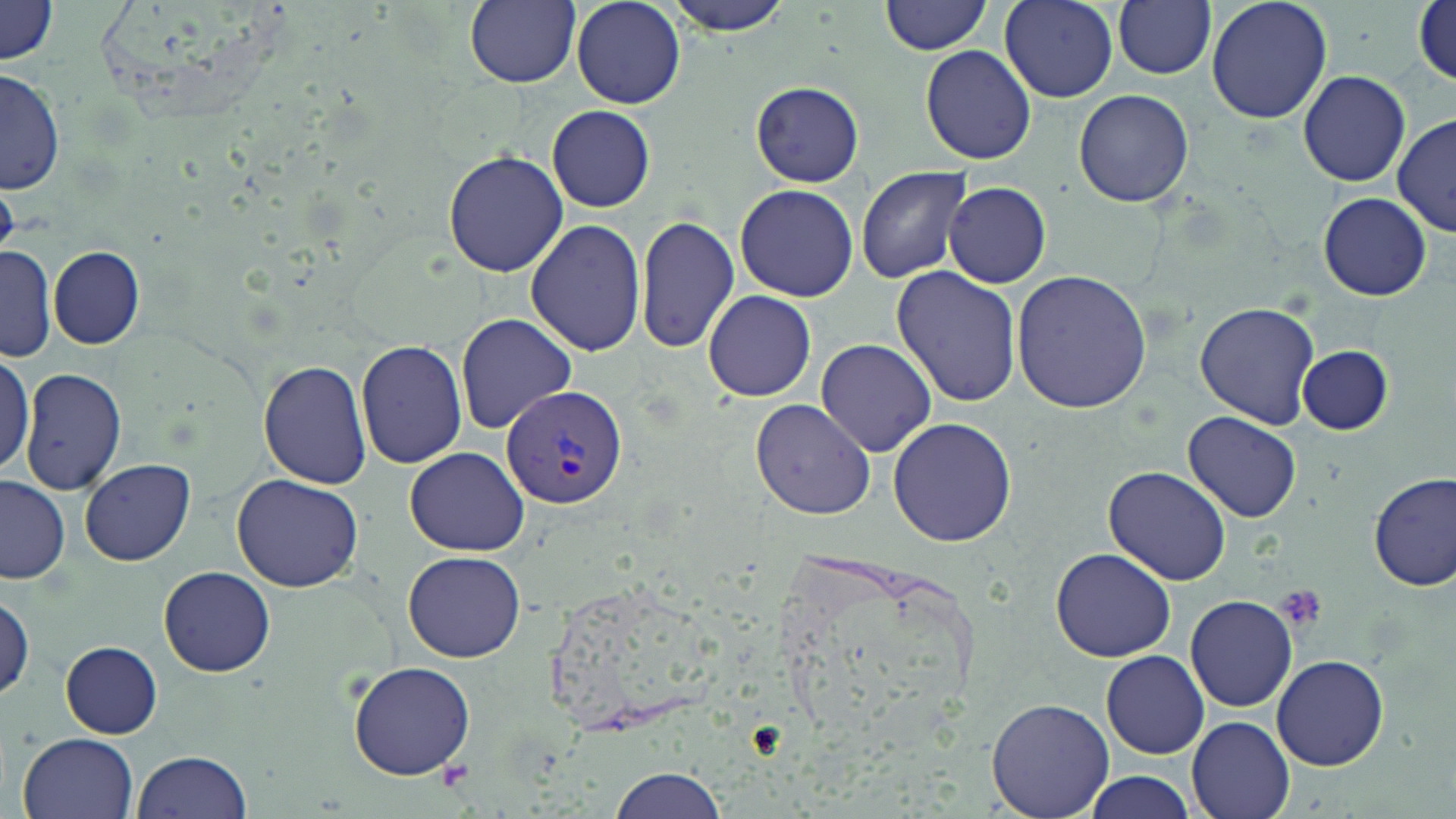

Approximate bounding boxes as named x1/y1/x2/y2 corners in pixels. Platelet locations: (x1=1271, y1=584, x2=1326, y2=632), (x1=436, y1=760, x2=474, y2=791). Plasmodium vivax-infected red blood cell locations: (x1=503, y1=384, x2=627, y2=507). Uninfected red blood cell locations: (x1=464, y1=0, x2=579, y2=88), (x1=663, y1=0, x2=796, y2=35), (x1=881, y1=0, x2=993, y2=55), (x1=996, y1=0, x2=1120, y2=104), (x1=1114, y1=0, x2=1215, y2=80), (x1=1205, y1=0, x2=1332, y2=125), (x1=1414, y1=0, x2=1455, y2=87), (x1=570, y1=1, x2=685, y2=108), (x1=1, y1=2, x2=59, y2=66), (x1=920, y1=45, x2=1035, y2=166), (x1=2, y1=68, x2=63, y2=195), (x1=1297, y1=69, x2=1412, y2=187), (x1=749, y1=79, x2=864, y2=188), (x1=1074, y1=89, x2=1194, y2=207), (x1=548, y1=105, x2=655, y2=212), (x1=1391, y1=115, x2=1454, y2=239), (x1=443, y1=149, x2=568, y2=278), (x1=856, y1=167, x2=972, y2=283), (x1=735, y1=182, x2=859, y2=302), (x1=944, y1=182, x2=1052, y2=287), (x1=1317, y1=192, x2=1431, y2=301), (x1=636, y1=213, x2=738, y2=354), (x1=525, y1=219, x2=647, y2=359), (x1=0, y1=244, x2=56, y2=365), (x1=48, y1=247, x2=145, y2=350), (x1=890, y1=266, x2=1023, y2=407), (x1=1011, y1=269, x2=1155, y2=415), (x1=703, y1=289, x2=817, y2=403), (x1=1194, y1=301, x2=1320, y2=429), (x1=455, y1=314, x2=578, y2=432), (x1=355, y1=339, x2=468, y2=468), (x1=815, y1=339, x2=938, y2=457), (x1=1299, y1=345, x2=1394, y2=435), (x1=0, y1=346, x2=32, y2=483), (x1=258, y1=359, x2=371, y2=489), (x1=20, y1=368, x2=128, y2=497), (x1=749, y1=398, x2=877, y2=519), (x1=1183, y1=412, x2=1302, y2=523), (x1=887, y1=417, x2=1018, y2=548), (x1=404, y1=447, x2=531, y2=556), (x1=80, y1=458, x2=195, y2=566), (x1=1103, y1=465, x2=1234, y2=586), (x1=1370, y1=471, x2=1455, y2=591), (x1=232, y1=473, x2=365, y2=591), (x1=1, y1=477, x2=69, y2=584), (x1=1050, y1=546, x2=1176, y2=662), (x1=403, y1=549, x2=527, y2=662), (x1=159, y1=566, x2=275, y2=676), (x1=0, y1=590, x2=33, y2=702), (x1=1185, y1=594, x2=1297, y2=712), (x1=61, y1=641, x2=163, y2=738), (x1=1102, y1=650, x2=1209, y2=759), (x1=1272, y1=653, x2=1390, y2=770), (x1=349, y1=662, x2=478, y2=780), (x1=987, y1=697, x2=1114, y2=818), (x1=1189, y1=716, x2=1296, y2=819), (x1=17, y1=732, x2=139, y2=819), (x1=132, y1=749, x2=254, y2=819), (x1=609, y1=766, x2=730, y2=818), (x1=1082, y1=772, x2=1198, y2=819). Slide-level diagnosis: Plasmodium vivax. Thin blood film. May-Grünwald-Giemsa stain. Image is 1456×819 pixels. 1000x magnification. Single field of view. Optical microscopy.